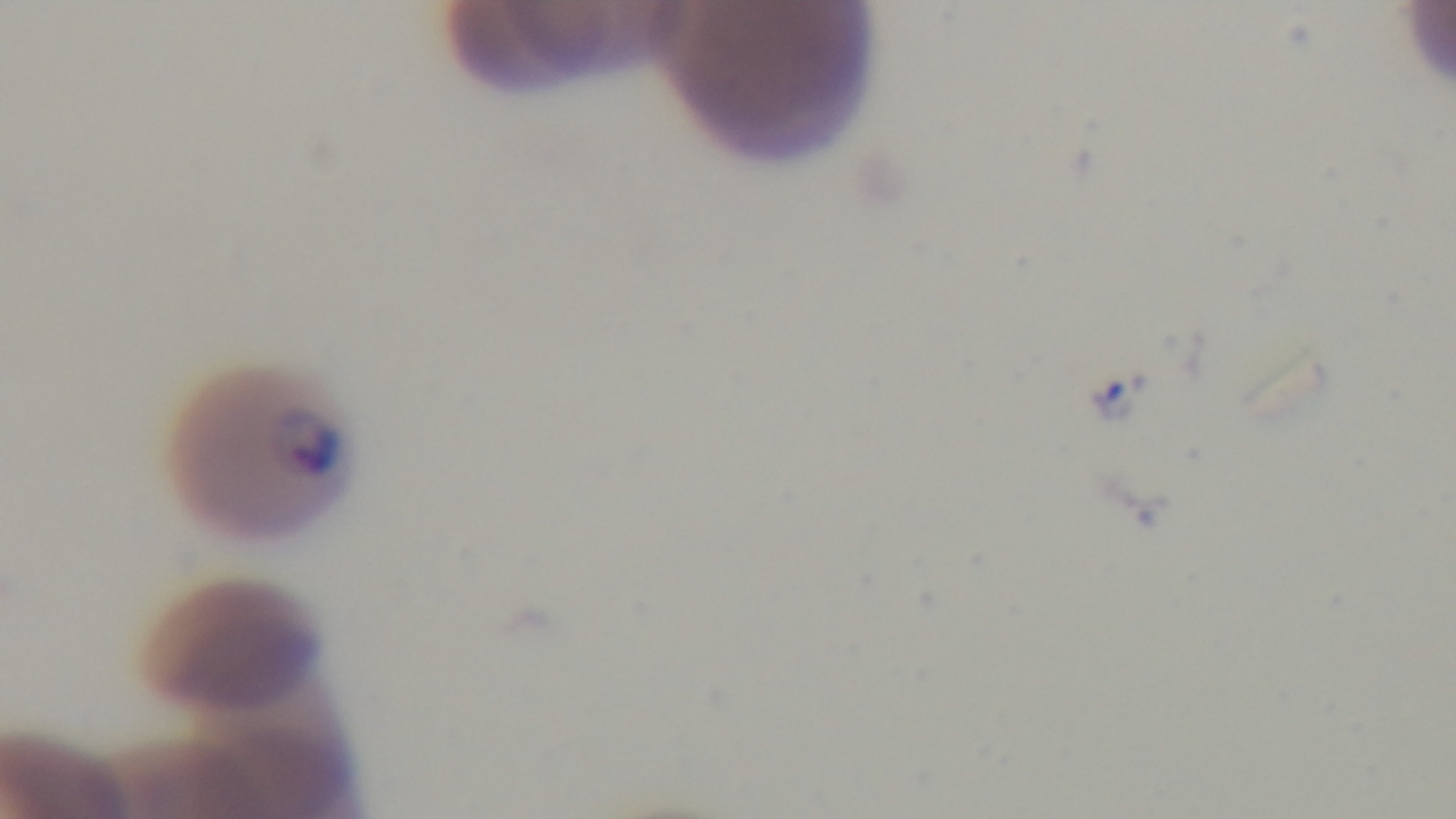
One field from the slide. Light microscopy. Preparation: thin smear. Giemsa-stained. Malaria status: positive. Mounted 4K digital camera. Oil-immersion objective, 100x.